Outline each uninfected red blood cell.
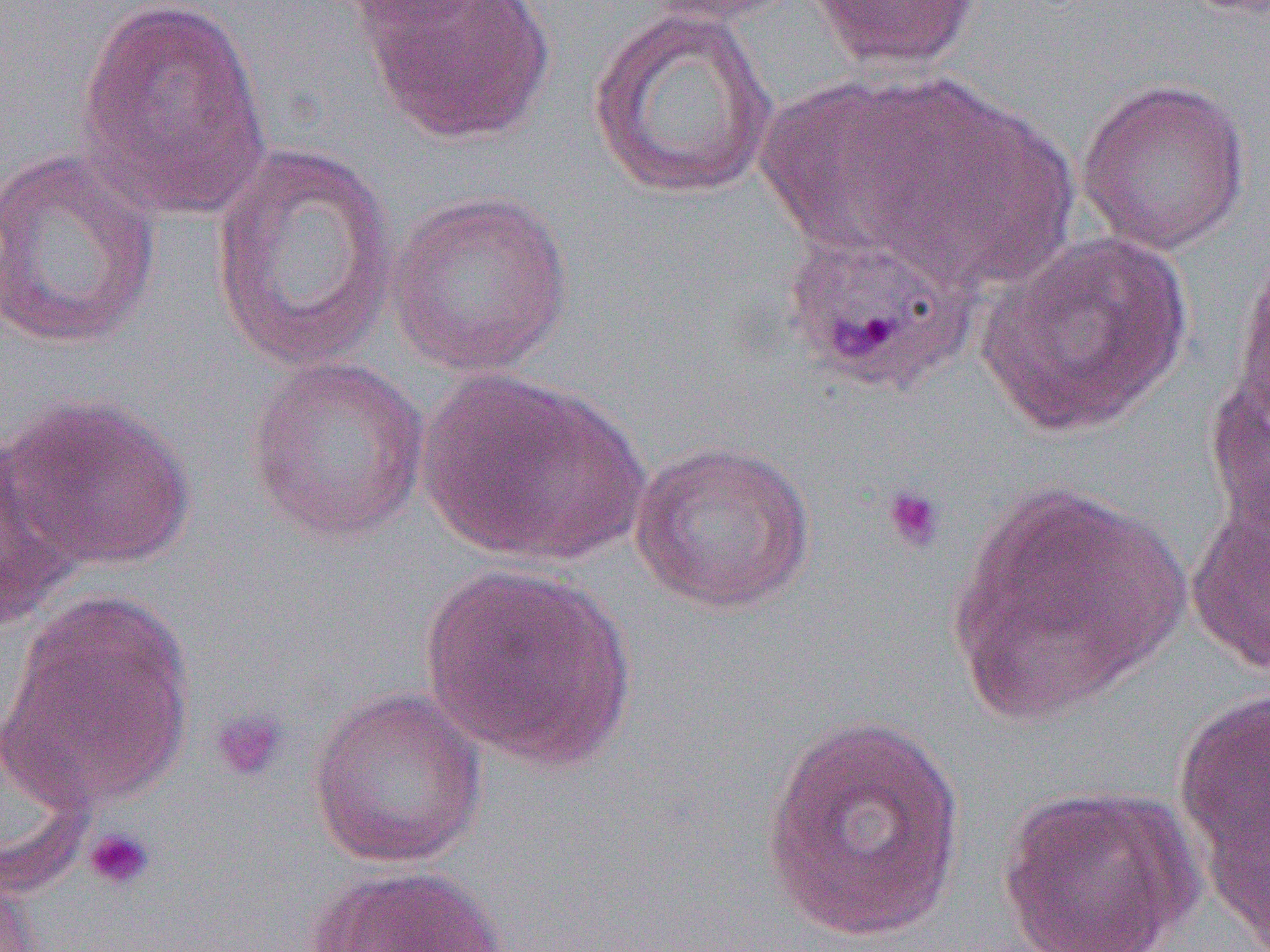
Approximate bounding boxes as [x1, y1, x2, y2] in pixels.
Uninfected red blood cells: [336, 0, 499, 34], [635, 0, 804, 26], [806, 0, 984, 74], [75, 1, 271, 221], [356, 1, 558, 146], [587, 6, 779, 200], [1076, 76, 1252, 255], [755, 77, 939, 252], [842, 83, 1074, 293], [208, 140, 399, 377], [0, 147, 162, 351], [386, 189, 575, 378], [781, 218, 981, 393], [977, 230, 1194, 437], [1235, 235, 1270, 429], [245, 354, 430, 544], [1203, 365, 1269, 540], [416, 368, 650, 566], [4, 393, 196, 573], [629, 439, 816, 615], [0, 448, 87, 629], [944, 482, 1190, 723], [1185, 501, 1270, 674], [417, 563, 640, 774], [4, 590, 194, 812], [1172, 684, 1270, 937], [307, 685, 489, 870], [761, 714, 967, 942], [0, 719, 95, 898], [998, 782, 1204, 952], [305, 863, 506, 952], [0, 868, 40, 952].

Summary:
  - Platelet locations: [880, 484, 946, 554], [207, 705, 289, 784], [82, 826, 156, 892]
  - Slide-level diagnosis: Plasmodium ovale
  - Modality: light microscopy
  - Preparation: thin blood film
  - Image size: 1270×952 pixels
  - Field of view: one of a larger specimen
  - Magnification: 1000x